Give the position of every Plasmodium parasite visible.
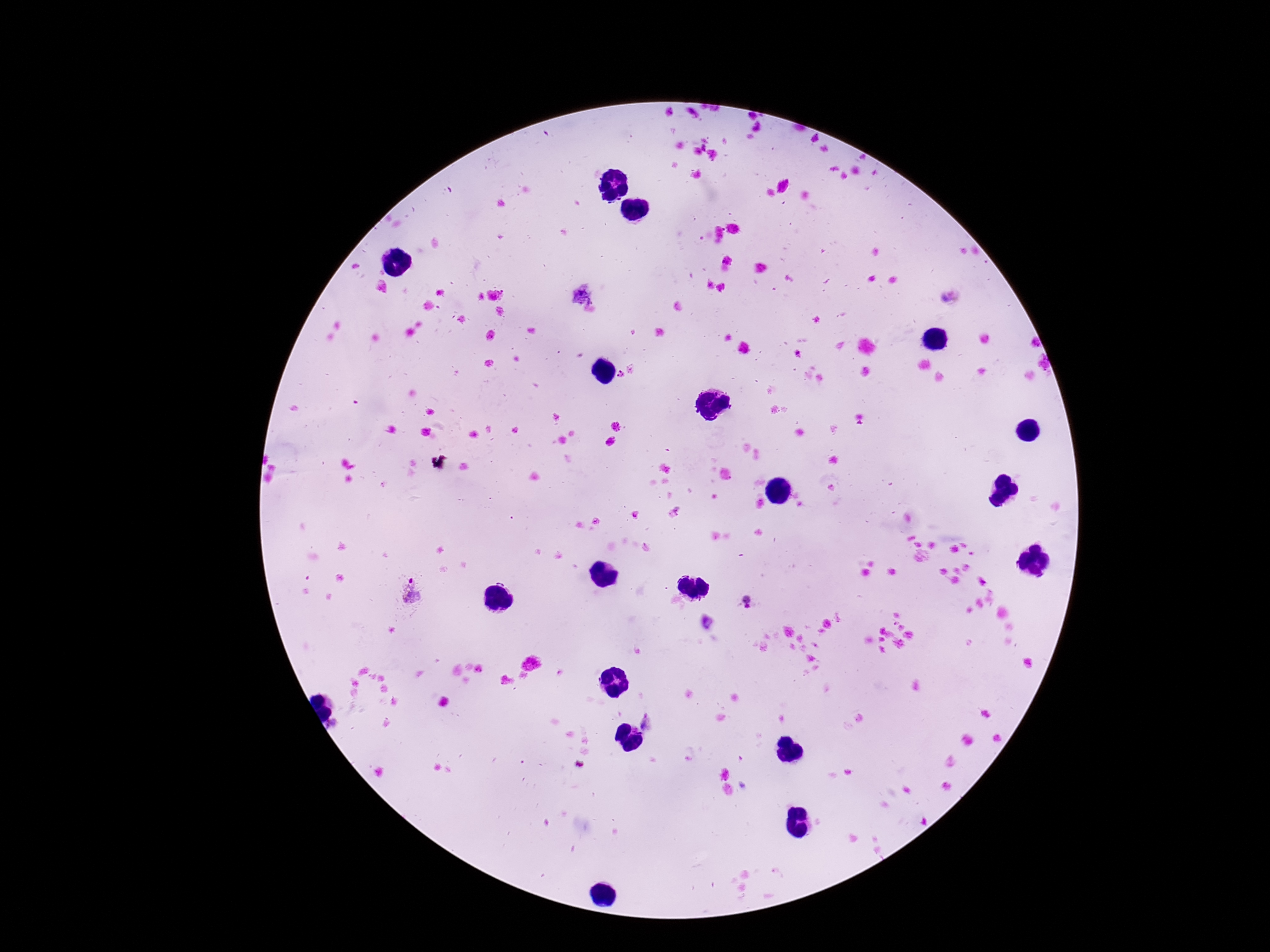
Approximate object centers, in pixels from the top-left corner.
Plasmodium parasites: (x=626, y=371), (x=414, y=591), (x=746, y=601), (x=646, y=722).

Photographed through the microscope eyepiece with a smartphone camera. One field from this slide. 100x magnification. Giemsa stain. Patient malaria status: infected. Thick blood smear. Image is 1270×952 pixels.